Point out each Plasmodium parasite.
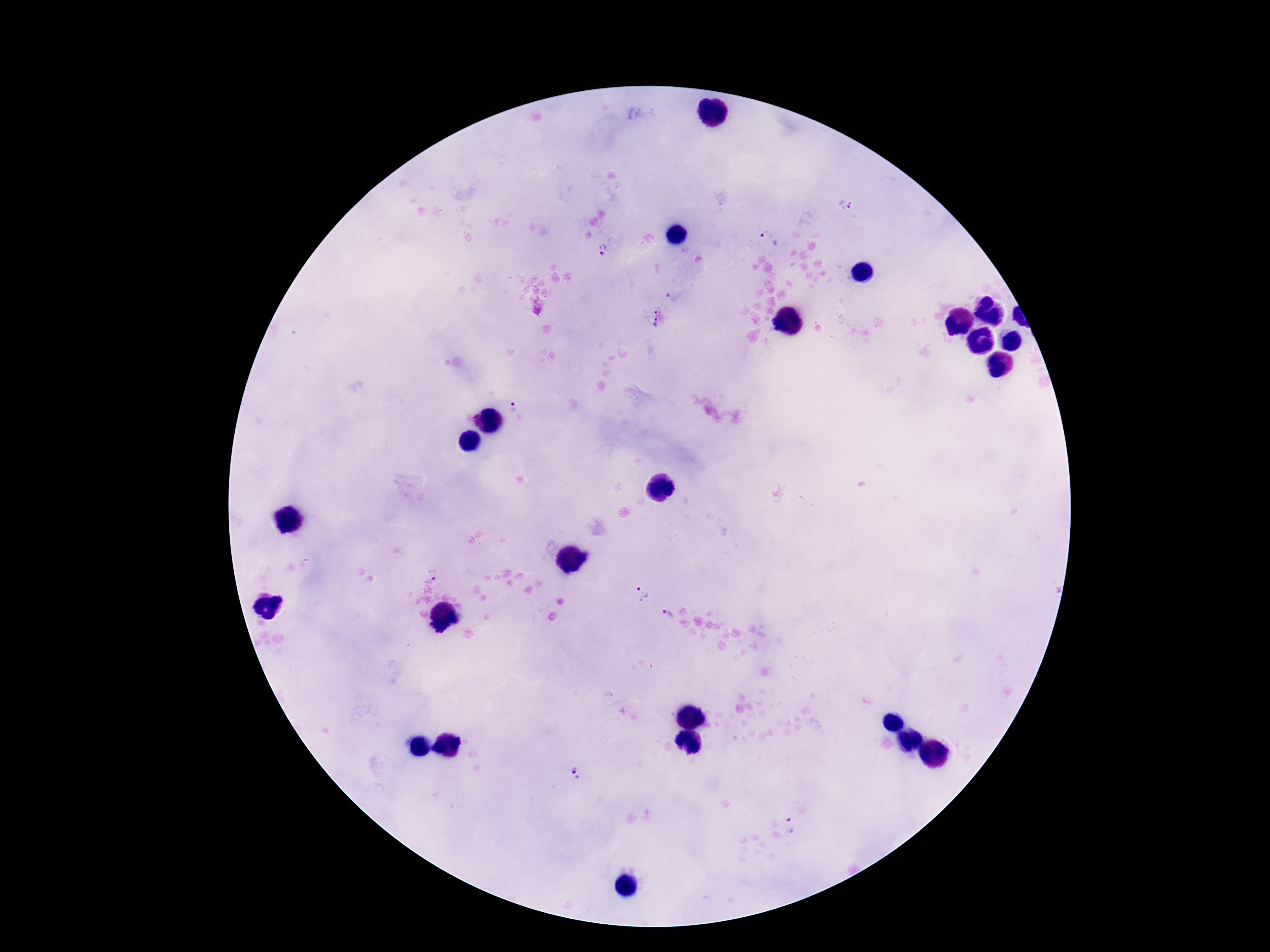

Approximate object centers, in pixels from the top-left corner.
Plasmodium parasites: (x=845, y=207), (x=770, y=236), (x=603, y=249), (x=673, y=298), (x=658, y=318), (x=521, y=405), (x=643, y=594), (x=670, y=616), (x=576, y=770), (x=791, y=825).

stain = Giemsa
patient malaria status = positive
image size = 1270×952 pixels
preparation = thick blood smear
capture = smartphone camera through the microscope eyepiece
magnification = 100x
field of view = one from this slide